Give a bounding box for every Plasmodium parasite, every leukocyte, and every artifact (stain precipitate or debris).
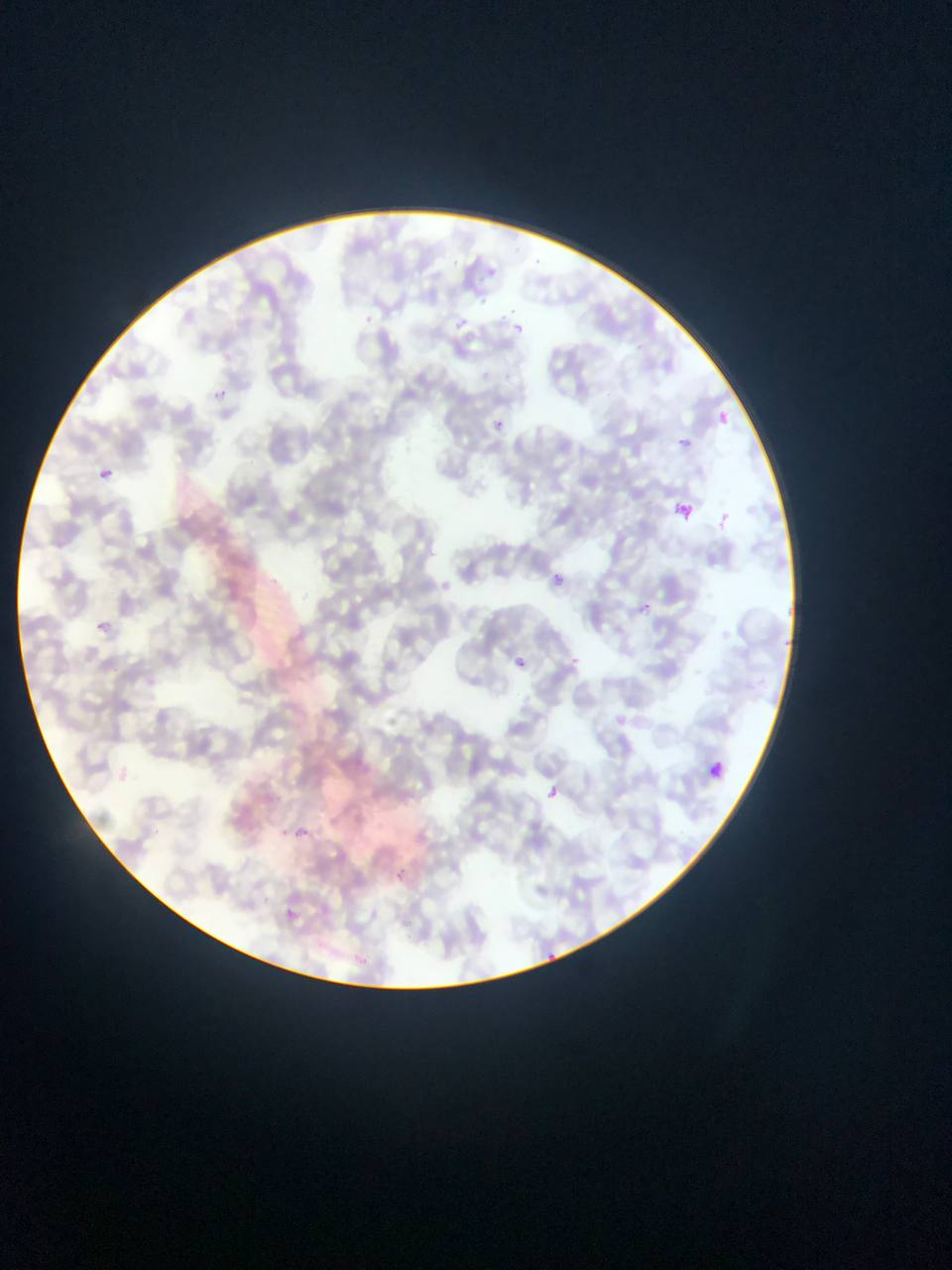
Approximate bounding boxes as left top right bottom in pixels.
Plasmodium parasites: 490 263 503 274; 477 296 494 303; 507 304 516 314; 361 312 378 329; 457 316 475 336; 513 320 523 344; 210 389 229 402; 712 411 732 428; 492 415 512 440; 673 433 698 452; 94 470 115 482; 550 569 573 592; 639 601 655 618; 95 621 109 633; 512 653 534 674; 547 786 564 800; 295 824 312 841; 394 864 411 891; 282 908 303 921; 539 948 555 961.
No leukocytes observed.

Summary:
  - Country: Ghana
  - Image size: 952×1270 pixels
  - Field of view: single
  - Preparation: thin blood film
  - Capture: mobile-phone photograph through a microscope